Give the position of every Plasmodium parasite.
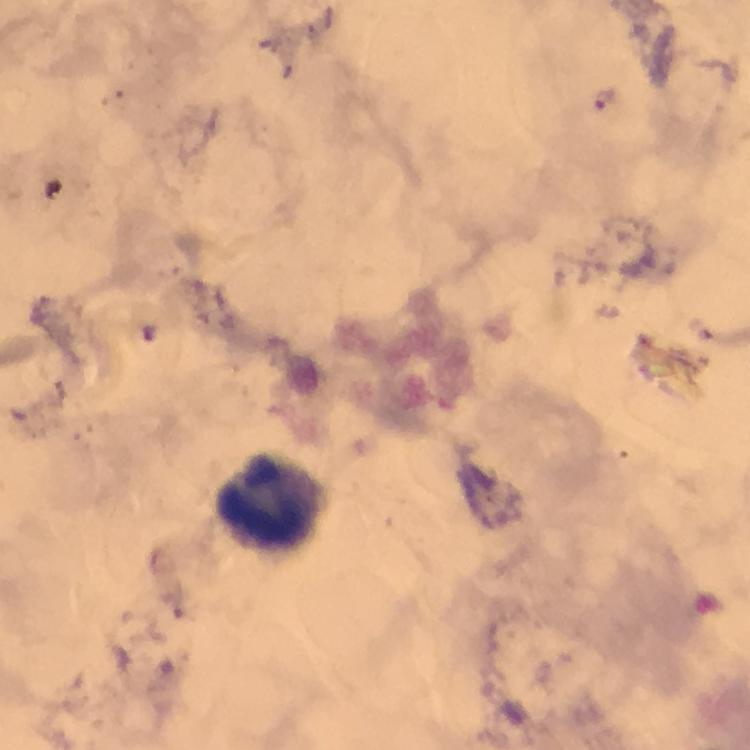

Approximate centers as [x, y] in pixels.
Plasmodium parasites: [604, 100].

Leukocyte locations: [272, 501]. 100x magnification. From a malaria diagnostic workup. Immersion oil applied. Smartphone photograph taken through a microscope. Cropped region of a single field of view. Thick blood film. Image is 750×750 pixels. Giemsa stain.